Assess this cell for malaria.
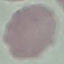

Uninfected.

image type = automatically extracted cell patch, resized to 64 × 64 pixels
preparation = thin blood film
stain = Giemsa
capture = smartphone through the microscope eyepiece